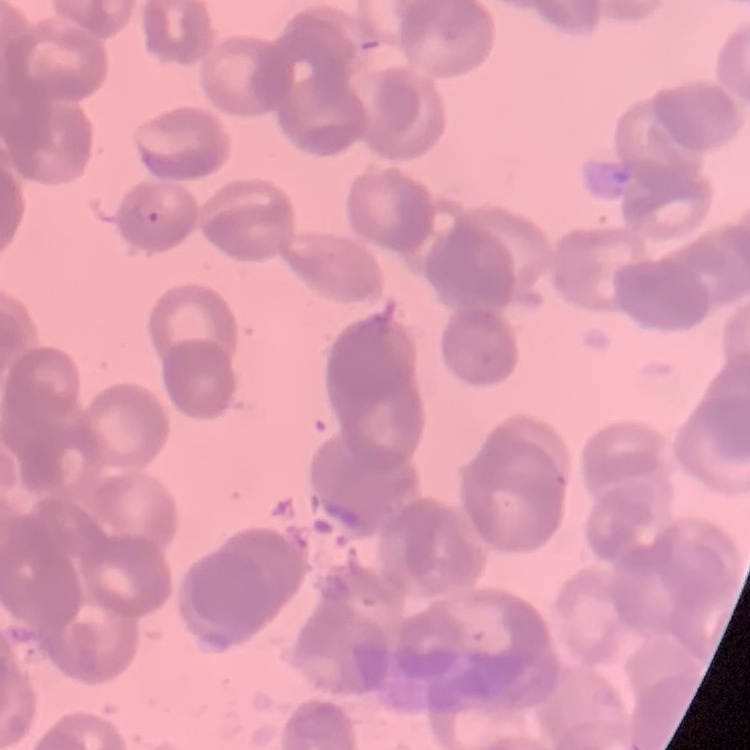
erythrocyte morphology = rouleaux formation
image type = square crop of a larger photomicrograph
preparation = thin blood film
stain = Field's or Giemsa